Assess this cell for malaria.
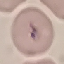
It is parasitized.

Summary:
  - Capture: smartphone camera at the microscope eyepiece
  - Preparation: thin blood film
  - Image type: automatically extracted cell patch, resized to 64 × 64 pixels
  - Stain: Giemsa